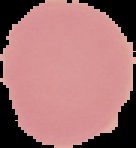
Segmented cell region on a black background. Result: no Plasmodium parasites detected. Image is 136×148 pixels. From a thin blood film.